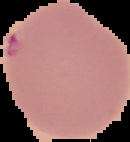

{
  "malaria_status": "uninfected",
  "image_type": "segmented cell region on a black background",
  "preparation": "thin blood smear",
  "image_size": "130×142 pixels"
}